State which cell type is depicted.
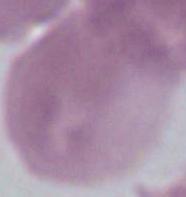

This is an erythrocyte.

1000x magnification. Photomicrograph.